Classify this cell by malaria status.
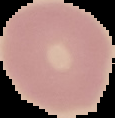
Uninfected.

Image is 115×118 pixels. From a thin blood smear. The area outside the segmented cell region is set to black.